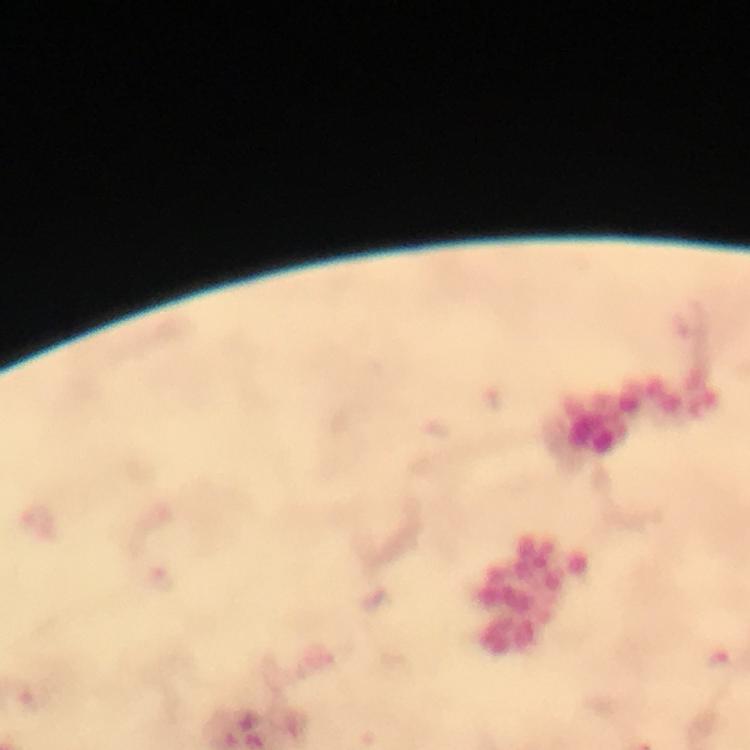
Approximate centers as (x, y) in pixels.
Summary:
  - Plasmodium parasite locations: (717, 663)
  - Context: from a malaria diagnostic workup
  - Capture: smartphone mounted on the microscope
  - Stain: Giemsa
  - Preparation: thick smear
  - Immersion oil: used
  - Magnification: 100x
  - Cropped from: a single field of view
  - Image size: 750×750 pixels